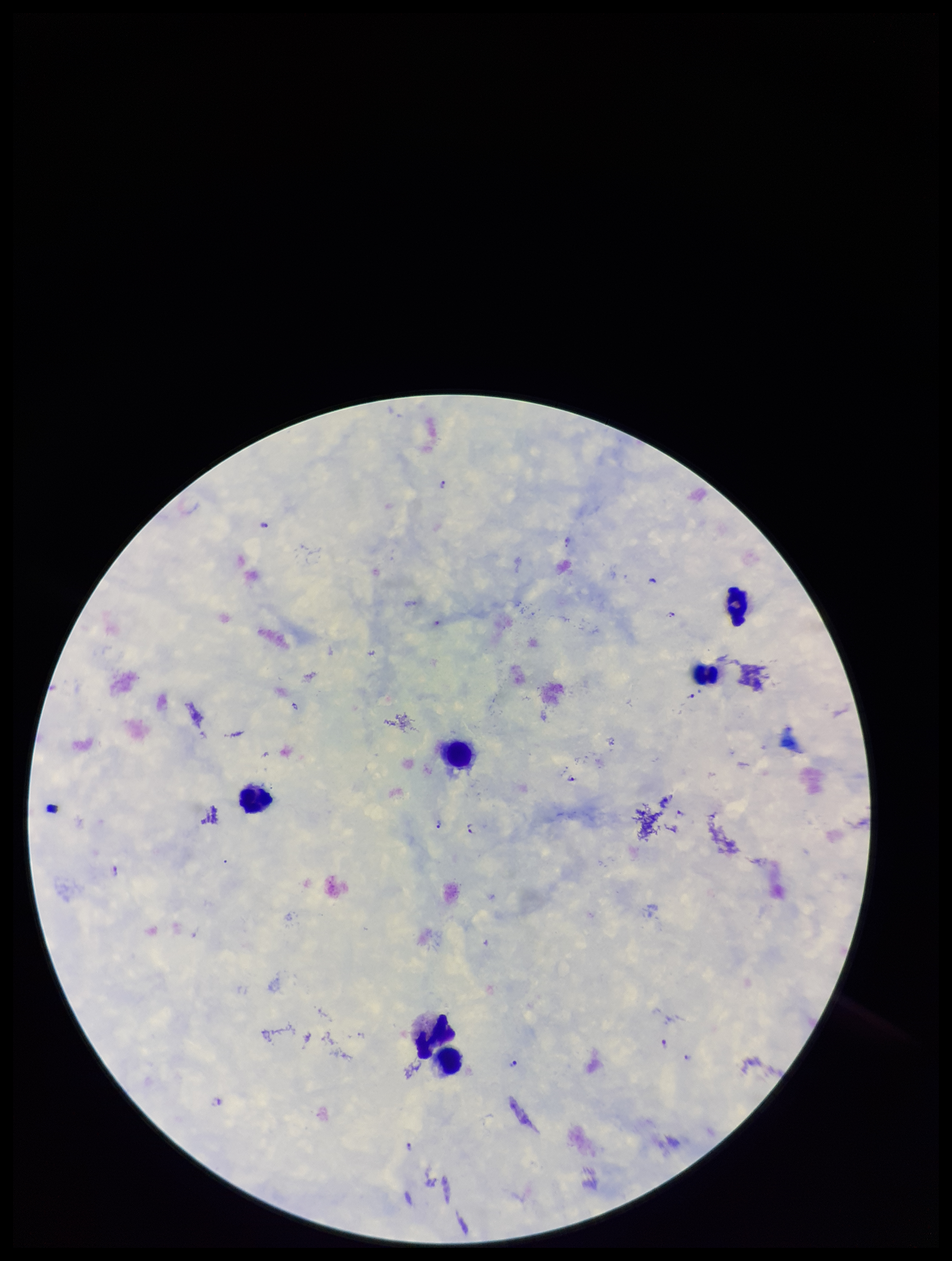

Summary:
  - Capture: smartphone photograph through the microscope eyepiece
  - Leukocyte count: 6
  - Preparation: thick blood smear
  - Stain: Giemsa
  - Patient malaria status: positive
  - Parasite count: 15
  - Species reported for this patient: Plasmodium falciparum
  - Image size: 952×1261 pixels
  - Plasmodium parasites: identified
  - Field of view: one from this slide